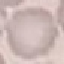

Result: no malaria parasites detected. Giemsa-stained preparation. Acquired by smartphone through the microscope eyepiece. Thin blood film. Cell patch, automatically extracted from a larger field of view and resized to 64 × 64 pixels.